Assess this cell for malaria.
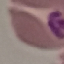

It is parasitized.

Summary:
  - Preparation: thin blood film
  - Capture: smartphone through the microscope eyepiece
  - Stain: Giemsa
  - Image type: automatically extracted cell patch, resized to 64 × 64 pixels